Give the position of every leukocyte visible.
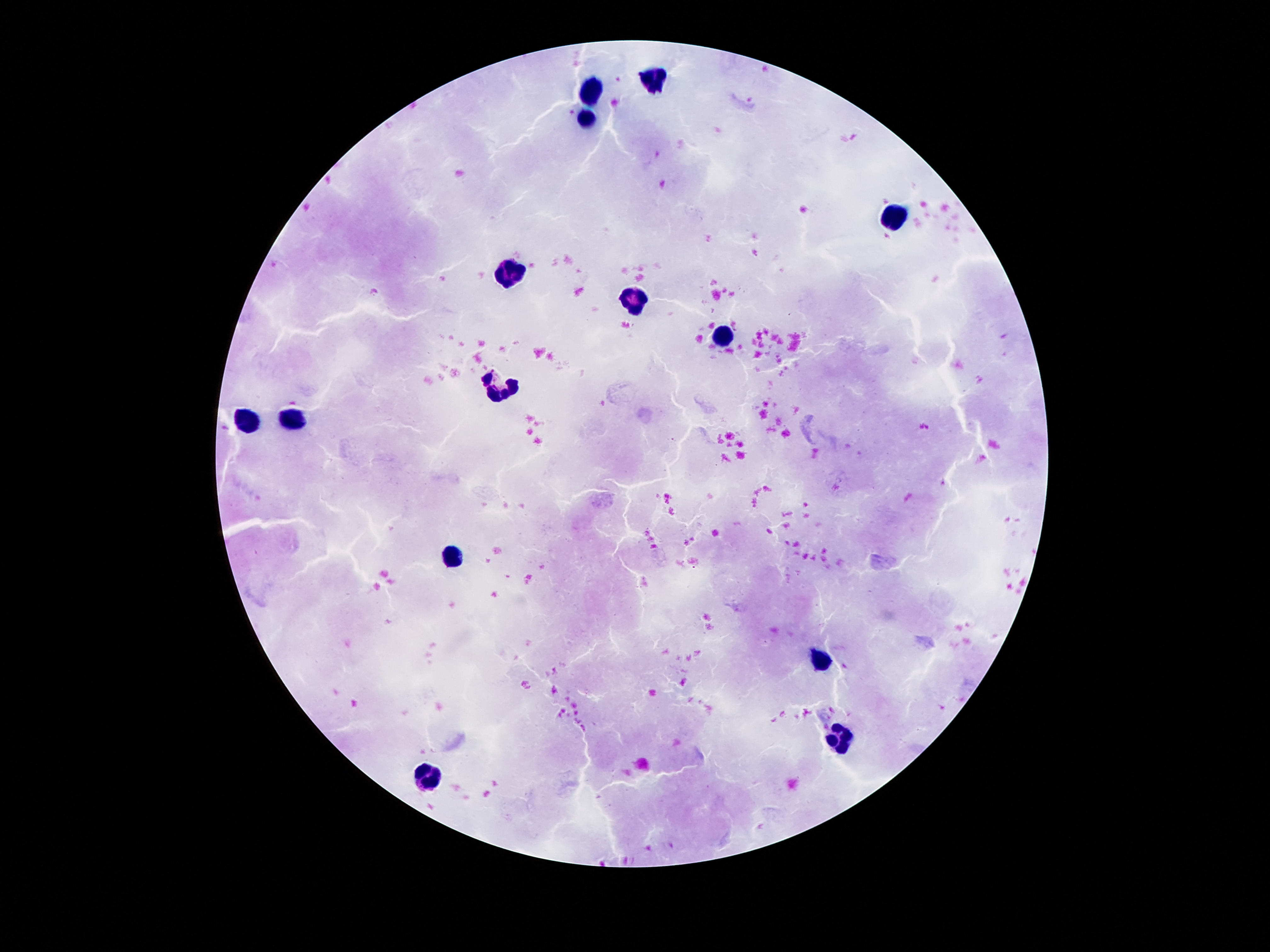

Approximate centers as {x, y} in pixels.
Leukocytes: {654, 79}, {591, 90}, {584, 117}, {894, 216}, {514, 271}, {635, 296}, {719, 341}, {497, 386}, {296, 417}, {245, 420}, {452, 558}, {819, 661}, {839, 738}, {428, 776}.

Thick peripheral-blood smear. Image is 1270×952 pixels. Giemsa-stained preparation. 100x magnification. Patient malaria status: negative. One field from this slide. Smartphone photograph taken through the microscope eyepiece.